Assess this cell for malaria.
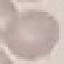

It is uninfected.

Acquired by smartphone through the microscope eyepiece. Automatically extracted cell patch, resized to 64 × 64 pixels. Thin blood film. Giemsa stain.